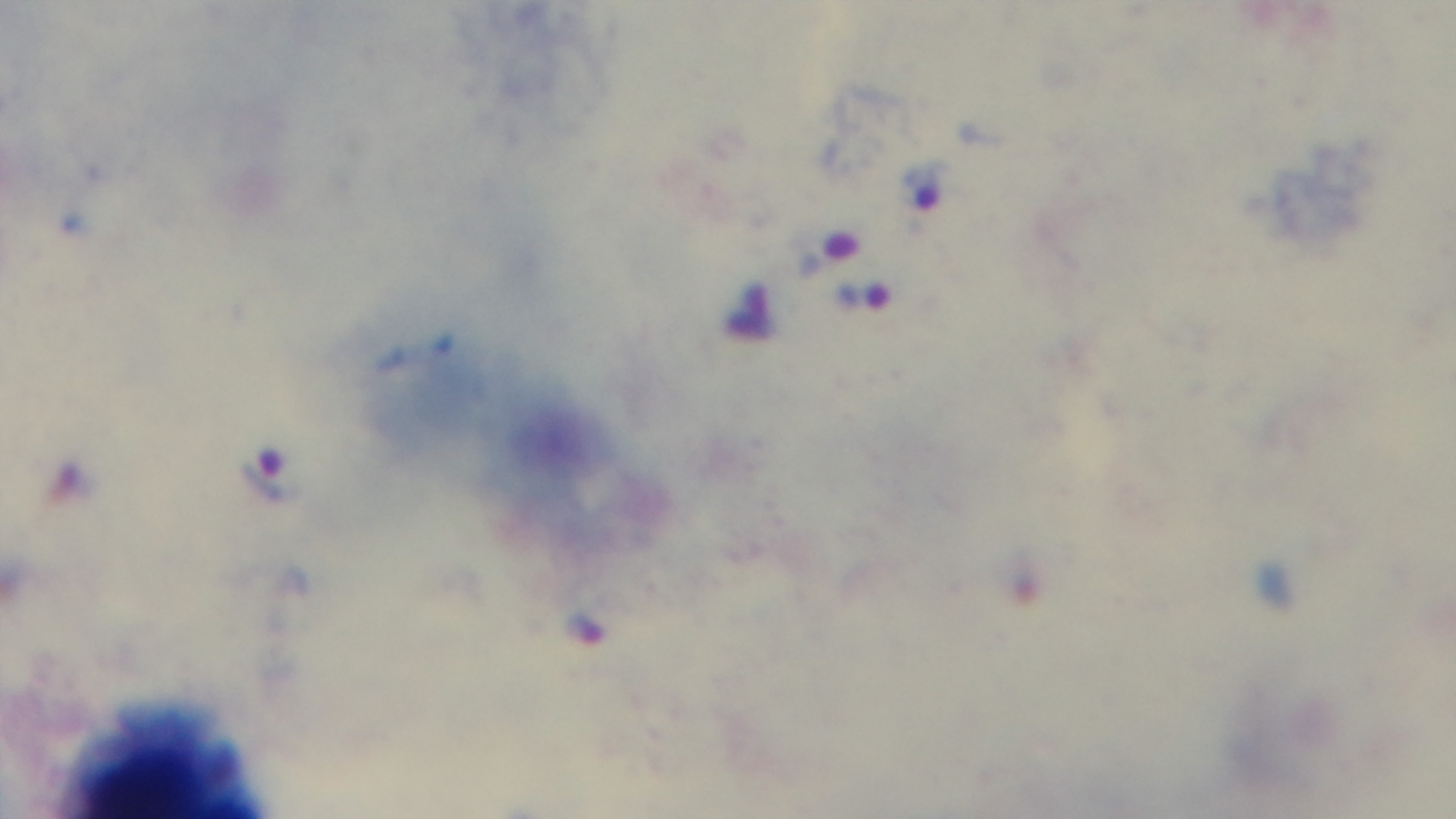

Malaria status: infected. Photomicrograph. Captured with a mounted 4K digital camera. Giemsa stain. Preparation: thick blood film. One field from the slide. 100x oil-immersion objective.